Assess this cell for malaria.
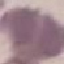
It is uninfected.

{
  "preparation": "thin smear",
  "capture": "smartphone through the microscope eyepiece",
  "stain": "Giemsa",
  "image_type": "cell patch, automatically extracted from a larger field of view and resized to 64 × 64 pixels"
}